Classify the preparation.
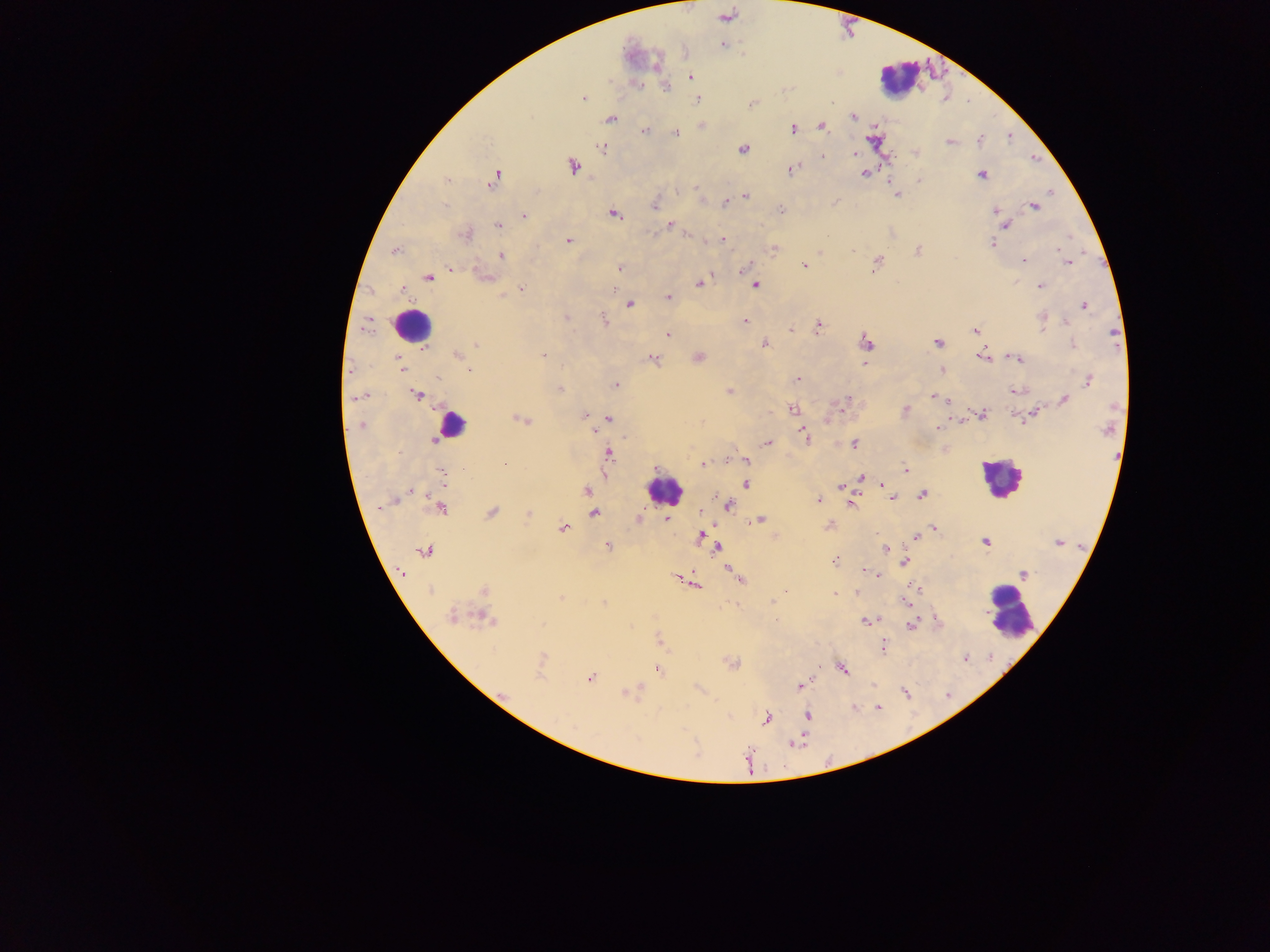

Thick blood smear.

{
  "image_size": "1270×952 pixels",
  "malaria_parasite_locations": "approximate centers as {x, y} in pixels: {723, 45}, {690, 76}, {666, 87}, {583, 97}, {697, 99}, {853, 117}, {610, 119}, {821, 127}, {793, 129}, {645, 130}, {675, 133}, {980, 140}, {949, 142}, {604, 147}, {743, 149}, {855, 153}, {573, 167}, {792, 168}, {863, 174}, {981, 174}, {495, 177}, {446, 180}, {920, 180}, {695, 188}, {677, 191}, {896, 195}, {746, 196}, {835, 201}, {725, 202}, {444, 206}, {654, 206}, {1034, 206}, {781, 209}, {995, 209}, {615, 214}, {999, 214}, {524, 216}, {670, 224}, {498, 226}, {1005, 226}, {687, 234}, {463, 236}, {722, 239}, {569, 240}, {992, 243}, {774, 249}, {395, 251}, {852, 251}, {918, 251}, {820, 253}, {502, 256}, {1024, 261}, {877, 262}, {1067, 262}, {804, 266}, {619, 268}, {451, 269}, {744, 271}, {485, 276}, {428, 277}, {700, 283}, {756, 285}, {1040, 286}, {403, 288}, {521, 289}, {504, 295}, {668, 297}, {629, 304}, {1085, 305}, {566, 317}, {1043, 319}, {605, 320}, {744, 322}, {1066, 323}, {819, 325}, {790, 329}, {975, 331}, {667, 334}, {865, 341}, {764, 343}, {938, 343}, {475, 344}, {1073, 344}, {425, 349}, {456, 355}, {542, 356}, {699, 357}, {398, 358}, {982, 358}, {1017, 358}, {652, 359}, {399, 363}, {865, 364}, {400, 368}, {468, 370}, {941, 370}, {438, 379}, {797, 380}, {1088, 381}, {616, 385}, {560, 389}, {1015, 390}, {729, 391}, {416, 395}, {933, 397}, {354, 399}, {847, 399}, {1065, 400}, {947, 401}, {792, 409}, {905, 411}, {584, 415}, {982, 415}, {1032, 415}, {607, 419}, {522, 420}, {827, 420}, {361, 426}, {938, 428}, {593, 430}, {804, 437}, {434, 440}, {767, 443}, {854, 444}, {609, 452}, {744, 460}, {703, 464}, {464, 469}, {906, 470}, {440, 472}, {861, 477}, {443, 483}, {746, 484}, {883, 485}, {840, 487}, {410, 489}, {587, 491}, {922, 495}, {887, 496}, {892, 498}, {818, 500}, {853, 504}, {727, 505}, {440, 508}, {491, 512}, {593, 513}, {529, 514}, {668, 519}, {759, 520}, {829, 526}, {562, 528}, {934, 528}, {702, 536}, {917, 536}, {985, 541}, {1058, 543}, {608, 546}, {716, 547}, {886, 549}, {425, 551}, {836, 560}, {904, 562}, {864, 570}, {1024, 574}, {877, 575}, {681, 578}, {738, 578}, {693, 583}, {917, 589}, {430, 590}, {483, 590}, {786, 592}, {834, 594}, {561, 598}, {906, 600}, {605, 604}, {452, 617}, {483, 618}, {776, 620}, {866, 620}, {911, 625}, {660, 641}, {883, 648}, {842, 668}, {658, 669}, {590, 678}, {800, 685}, {628, 693}, {807, 716}, {767, 718}, {794, 744}",
  "field_of_view": "single",
  "country": "Ghana",
  "leukocyte_locations": "approximate centers as {x, y} in pixels: {897, 78}, {412, 325}, {451, 425}, {1000, 478}, {664, 489}, {1011, 612}",
  "capture": "mobile-phone photograph through a microscope"
}